Assess the morphology of the red blood cells.
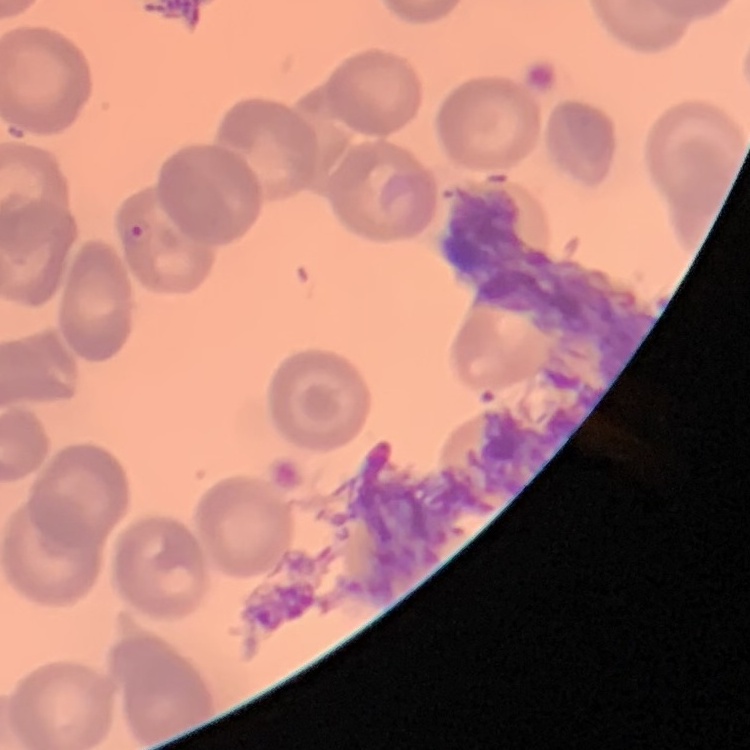

No rouleaux formation.

Thin peripheral smear. Field's or Giemsa stain. One tile cut from a larger photomicrograph.